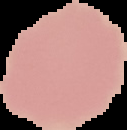

result: negative for Plasmodium parasites
image_size: 127×130 pixels
preparation: thin blood film
image_type: segmented cell region on a black background